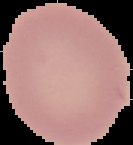
Summary:
  - Result: no Plasmodium parasites detected
  - Image size: 133×145 pixels
  - Preparation: thin blood smear
  - Image type: segmented cell region on a black background